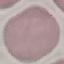
Malaria status: uninfected. Giemsa-stained preparation. Thin blood smear. Acquired by smartphone through the microscope eyepiece. Cell patch, automatically extracted from a larger field of view and resized to 64 × 64 pixels.